Assess the morphology of the erythrocytes.
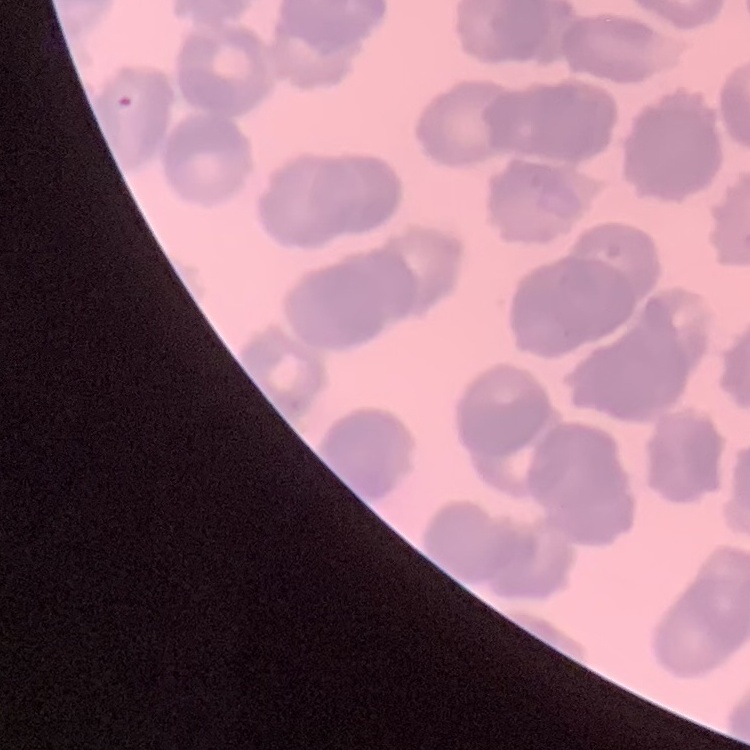

Rouleaux formation.

Summary:
  - Preparation: thin peripheral smear
  - Stain: Field's or Giemsa
  - Image type: one tile cut from a larger photomicrograph